Identify the parasite.
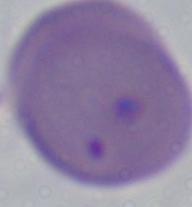
This is Babesia.

magnification: 1000x
modality: photomicrograph